Point out each Plasmodium parasite.
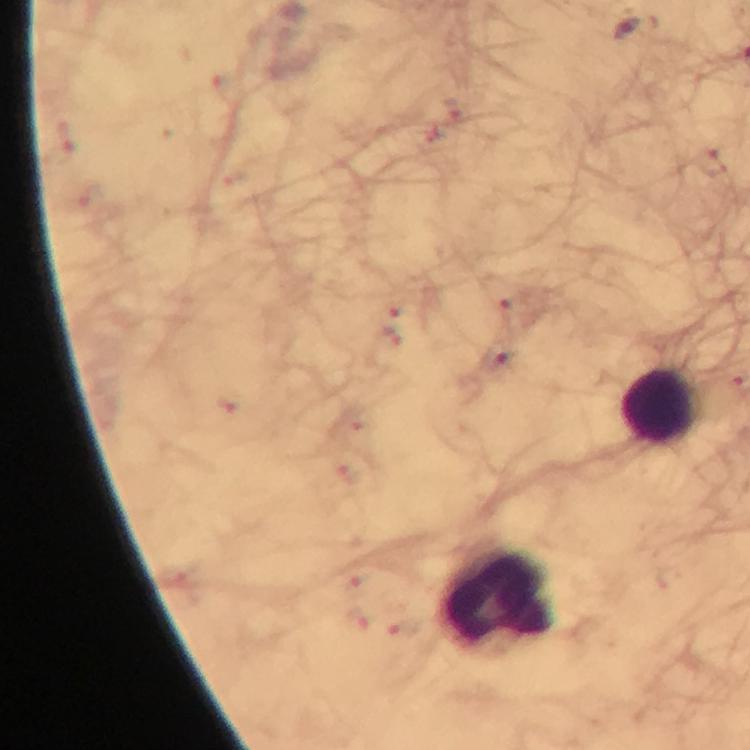
Approximate centers as (x, y) in pixels.
Plasmodium parasites: (497, 358).

Summary:
  - Leukocyte locations: (658, 404), (498, 596)
  - Magnification: 100x
  - Cropped from: a single field of view
  - Stain: Giemsa
  - Capture: smartphone camera through the microscope
  - Preparation: thick blood film
  - Immersion oil: applied
  - Context: from a malaria diagnostic workup
  - Image size: 750×750 pixels